Point out each Plasmodium parasite.
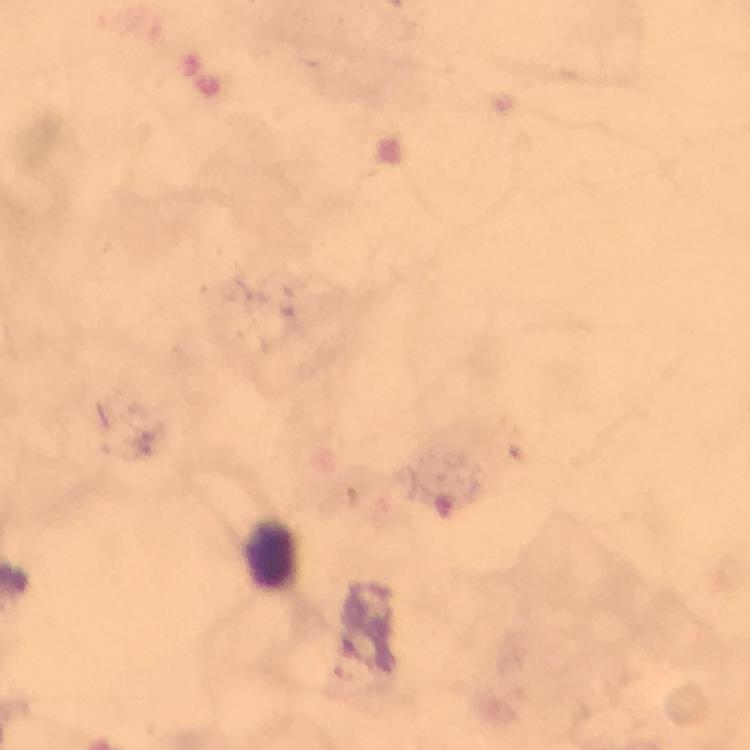

No Plasmodium parasites detected.

Approximate object centers, in pixels from the top-left corner.
Summary:
  - Leukocyte locations: (x=271, y=554)
  - Preparation: thick blood smear
  - Stain: Giemsa
  - Image size: 750×750 pixels
  - Immersion oil: applied
  - Context: from a malaria diagnostic workup
  - Cropped from: one field of view
  - Capture: smartphone mounted on the microscope
  - Magnification: 100x